Classify this cell by malaria status.
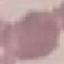

Uninfected.

Cell patch, automatically extracted from a larger field of view and resized to 64 × 64 pixels. Photographed with a smartphone camera at the microscope eyepiece. Thin blood smear. Giemsa stain.